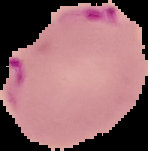

Result: Plasmodium parasites identified. From a thin blood film. Image is 148×151 pixels. Segmented cell region on a black background.